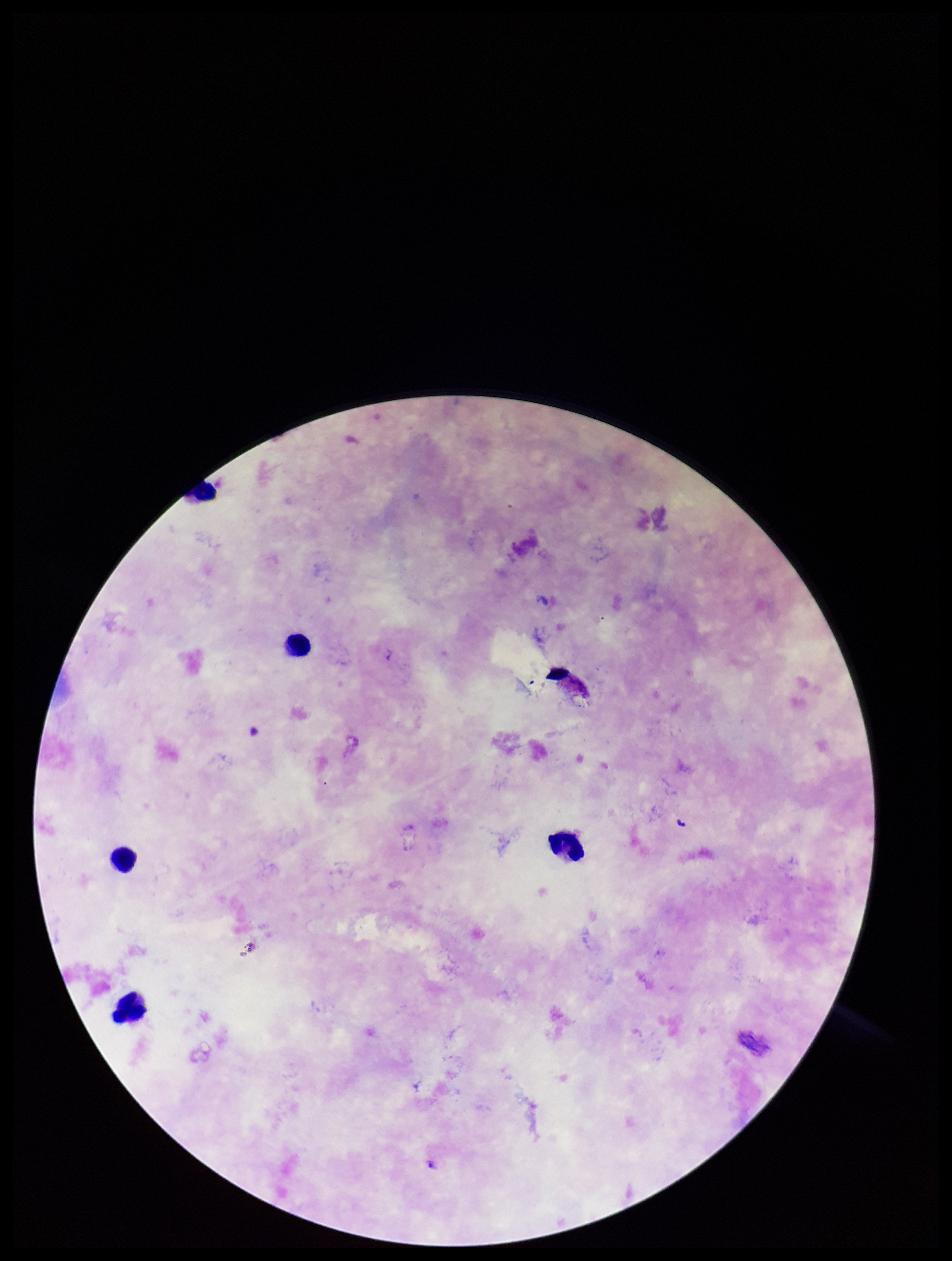
Summary:
  - Image size: 952×1261 pixels
  - Capture: smartphone photograph through the microscope eyepiece
  - Leukocyte count: 5
  - Plasmodium parasites: none detected
  - Preparation: thick
  - Field of view: one from this slide
  - Stain: Giemsa
  - Patient malaria status: positive
  - Parasite count: 0
  - Species reported for this patient: Plasmodium falciparum